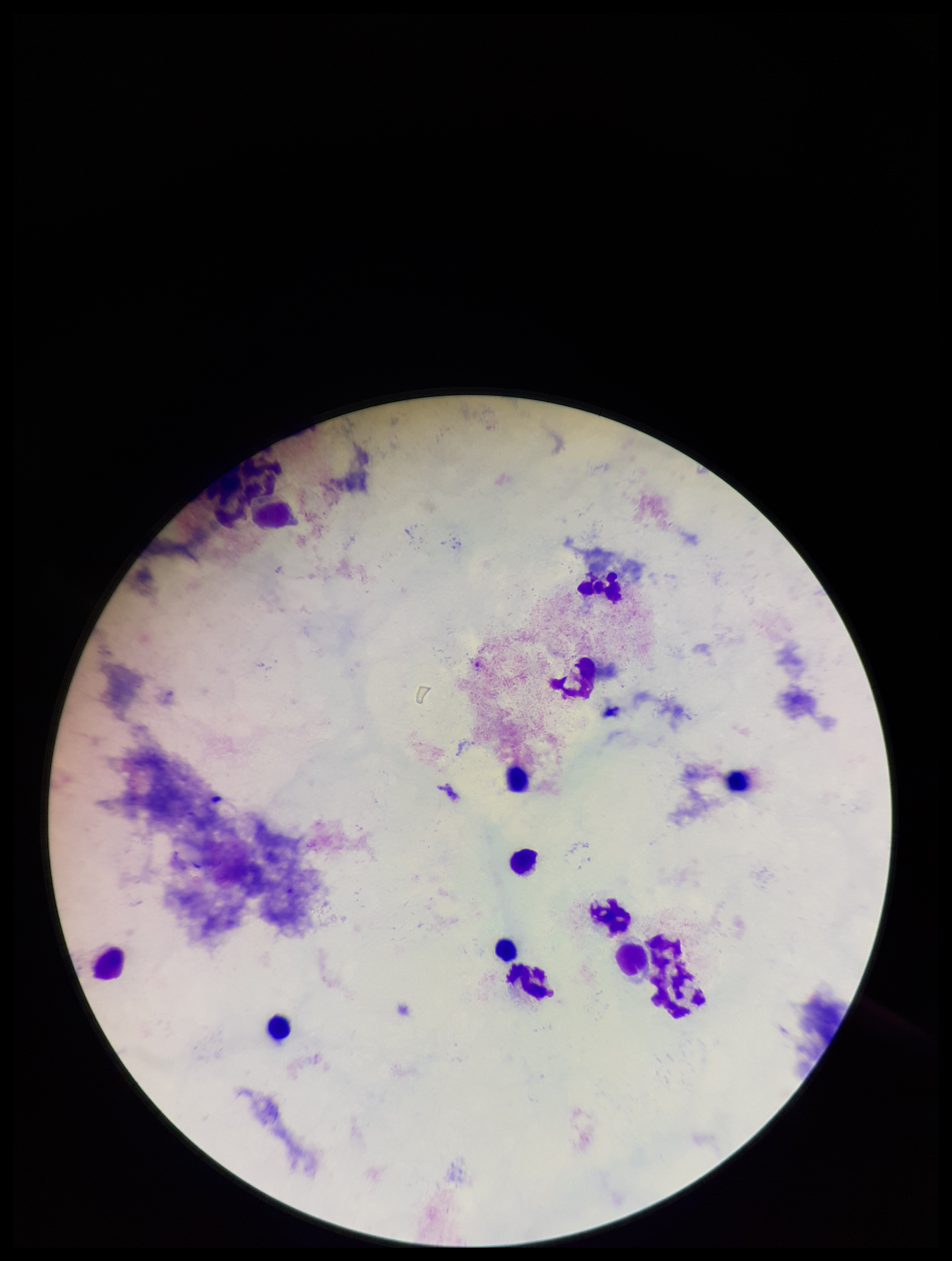

Preparation: thick blood smear. Giemsa stain. Parasite count: 0. Leukocyte count: 12. Image is 952×1261 pixels. Single field of view. Smartphone photograph taken through the eyepiece of a microscope. Patient malaria status: negative. Plasmodium parasites: none identified.